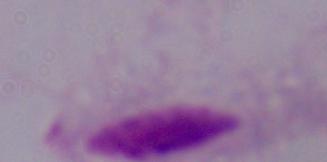

Summary:
  - Magnification: 1000x
  - Identification: trichomonad
  - Modality: photomicrograph